Classify this cell by malaria status.
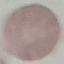
It is uninfected.

preparation: thin blood film
stain: Giemsa
image_type: automatically extracted cell patch, resized to 64 × 64 pixels
capture: smartphone through the microscope eyepiece